Identify the blood parasite species.
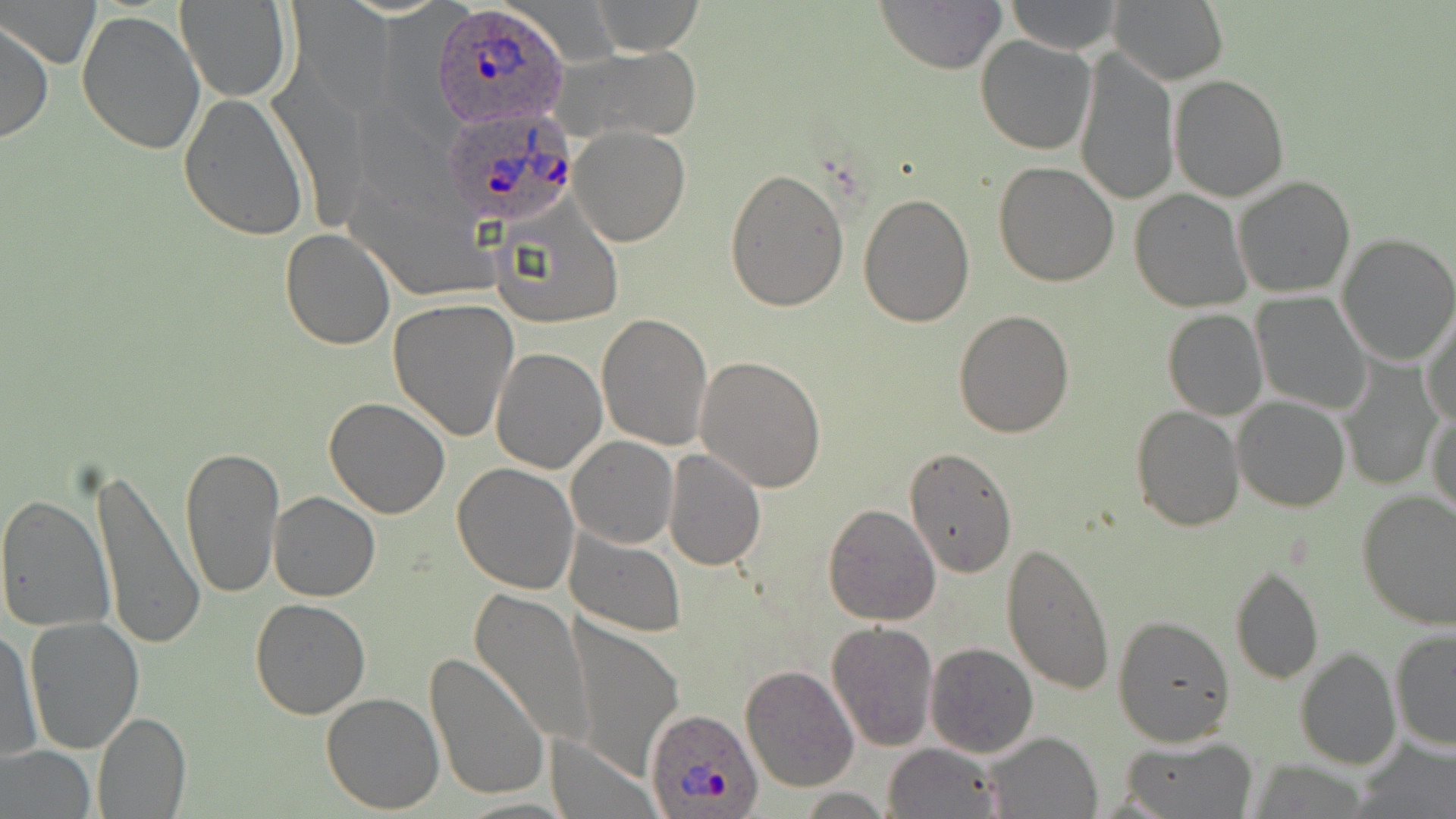
Plasmodium ovale.

Summary:
  - Coordinate format: approximate bounding boxes as [x1, y1, x2, y2] in pixels
  - Plasmodium ovale-infected red blood cell locations: [431, 3, 570, 130], [440, 108, 578, 236], [645, 709, 762, 819]
  - Uninfected red blood cell locations: [2, 0, 98, 68], [176, 0, 291, 104], [289, 0, 394, 109], [874, 0, 1006, 74], [1002, 0, 1126, 54], [1111, 0, 1228, 86], [583, 1, 705, 53], [75, 8, 205, 154], [0, 17, 52, 146], [975, 35, 1097, 154], [548, 42, 705, 146], [1072, 44, 1180, 209], [267, 63, 370, 232], [1170, 76, 1290, 202], [178, 93, 310, 240], [568, 125, 690, 246], [992, 162, 1121, 287], [724, 166, 850, 312], [1232, 175, 1358, 299], [858, 190, 976, 327], [1129, 190, 1251, 312], [490, 201, 625, 331], [280, 229, 395, 350], [1334, 233, 1456, 366], [1251, 293, 1372, 415], [387, 298, 520, 441], [1421, 308, 1456, 429], [952, 309, 1074, 438], [1163, 309, 1267, 420], [596, 312, 712, 451], [491, 346, 607, 474], [693, 354, 826, 493], [1337, 357, 1443, 491], [1232, 396, 1352, 512], [323, 397, 453, 518], [1428, 402, 1456, 526], [1130, 406, 1244, 531], [566, 435, 678, 549], [180, 445, 285, 600], [904, 446, 1017, 577], [662, 448, 768, 571], [88, 460, 202, 652], [452, 463, 580, 594], [268, 491, 379, 602], [1357, 492, 1456, 630], [0, 493, 117, 632], [823, 503, 941, 625], [564, 529, 686, 637], [1001, 542, 1115, 696], [1230, 563, 1323, 687], [469, 589, 594, 747], [248, 598, 373, 720], [1113, 613, 1236, 747], [23, 617, 145, 755], [568, 618, 682, 783], [825, 622, 940, 752], [1, 627, 41, 762], [1389, 628, 1456, 751], [925, 641, 1039, 758], [1296, 647, 1402, 770], [424, 653, 547, 803], [739, 663, 858, 793], [321, 691, 444, 814], [92, 711, 190, 818], [984, 731, 1102, 817], [1120, 735, 1257, 818], [1353, 736, 1455, 818], [546, 738, 657, 817], [882, 743, 1006, 819], [0, 746, 96, 819], [795, 787, 892, 816]
  - Preparation: thin blood smear
  - Stain: May-Grünwald-Giemsa
  - Field of view: single
  - Magnification: 1000x
  - Modality: light microscopy
  - Image size: 1456×819 pixels